Classify this cell by malaria status.
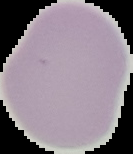

It is uninfected.

preparation = thin blood film
image type = cell region segmented out of the field of view; surrounding area masked to black
image size = 133×154 pixels